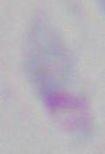

Toxoplasma gondii is shown. Captured at 1000x magnification. Micrograph.